Classify this cell by malaria status.
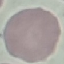
It is uninfected.

capture: smartphone camera at the microscope eyepiece
preparation: thin blood film
stain: Giemsa
image_type: automatically extracted cell patch, resized to 64 × 64 pixels